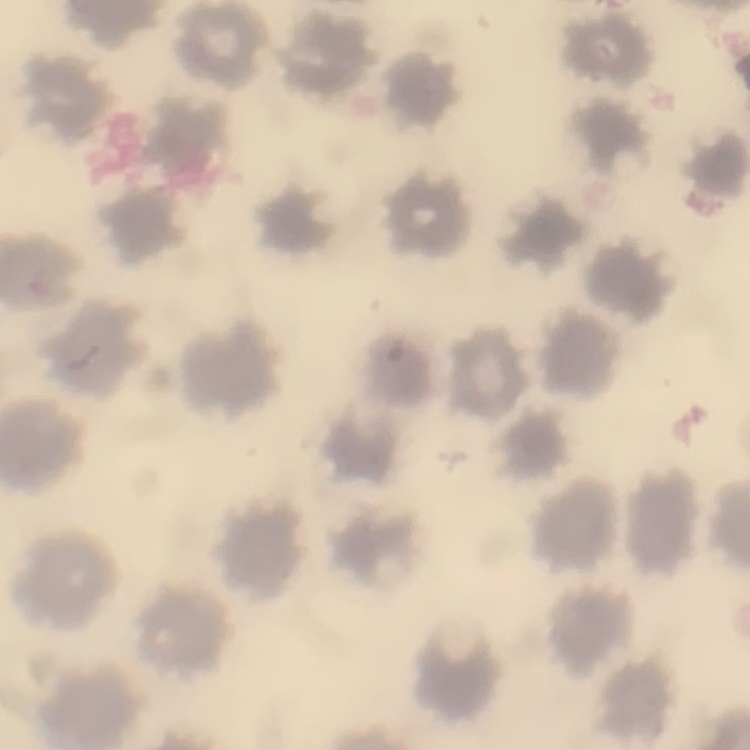 The red blood cells show no rouleaux formation. Field's or Giemsa stain. Thin peripheral smear. One tile cut from a larger photomicrograph.